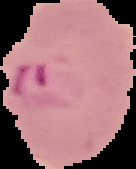

The area outside the segmented cell region is set to black. Image is 136×169 pixels. From a thin blood film. Result: Plasmodium parasites detected.